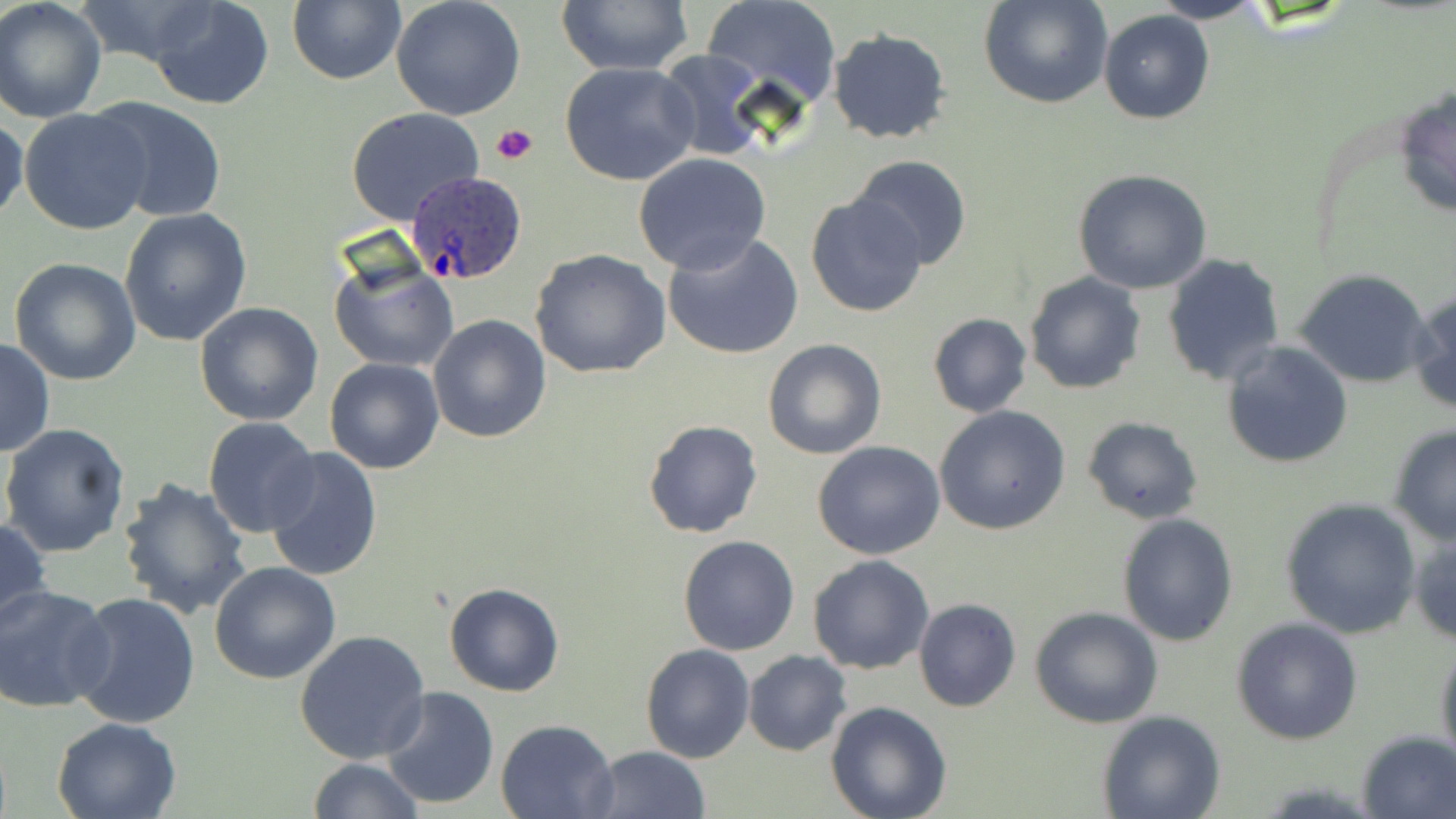
Summary:
  - Coordinate format: approximate bounding boxes as [x1, y1, x2, y2] in pixels
  - Platelet locations: [492, 123, 537, 166]
  - Plasmodium ovale-infected red blood cell locations: [404, 167, 531, 286]
  - Uninfected red blood cell locations: [0, 0, 107, 124], [73, 0, 224, 69], [147, 0, 275, 110], [391, 0, 526, 121], [556, 0, 696, 75], [701, 0, 843, 109], [978, 0, 1114, 110], [1149, 0, 1272, 24], [286, 1, 406, 86], [1099, 11, 1216, 125], [827, 28, 954, 146], [653, 50, 771, 161], [559, 61, 700, 186], [1393, 84, 1456, 220], [93, 98, 229, 222], [19, 107, 154, 235], [347, 109, 483, 225], [0, 116, 26, 225], [633, 153, 773, 275], [848, 154, 972, 270], [1072, 168, 1213, 294], [806, 194, 928, 317], [120, 208, 253, 346], [662, 231, 805, 361], [530, 248, 670, 379], [329, 253, 459, 373], [1160, 254, 1285, 387], [9, 257, 141, 387], [1295, 270, 1433, 388], [1023, 271, 1146, 395], [1408, 289, 1456, 416], [195, 301, 324, 426], [427, 313, 550, 442], [927, 313, 1033, 418], [0, 338, 54, 458], [762, 338, 887, 459], [1221, 342, 1353, 469], [325, 357, 446, 474], [935, 406, 1072, 535], [203, 416, 320, 538], [1081, 417, 1202, 525], [643, 419, 763, 538], [1387, 423, 1456, 547], [1, 424, 132, 557], [812, 441, 945, 561], [262, 445, 382, 582], [117, 476, 253, 620], [1280, 497, 1422, 638], [1117, 513, 1238, 647], [0, 516, 51, 633], [1409, 523, 1456, 647], [678, 536, 800, 656], [808, 555, 935, 674], [210, 562, 341, 684], [443, 582, 565, 698], [0, 587, 114, 714], [69, 591, 200, 729], [913, 599, 1023, 713], [1029, 605, 1165, 730], [1231, 618, 1363, 744], [295, 629, 430, 764], [1434, 638, 1456, 776], [641, 645, 755, 764], [744, 650, 852, 757], [380, 685, 500, 808], [826, 701, 952, 819], [1096, 711, 1225, 819], [51, 716, 185, 819], [496, 718, 620, 818], [1356, 730, 1456, 818], [587, 746, 710, 819], [307, 756, 424, 819]
  - Slide-level diagnosis: Plasmodium ovale
  - Magnification: 1000x
  - Field of view: single
  - Modality: light microscopy
  - Preparation: thin blood smear
  - Stain: May-Grünwald-Giemsa
  - Image size: 1456×819 pixels